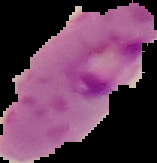
Summary:
  - Image size: 157×163 pixels
  - Image type: segmented cell region on a black background
  - Preparation: thin blood smear
  - Malaria status: parasitized